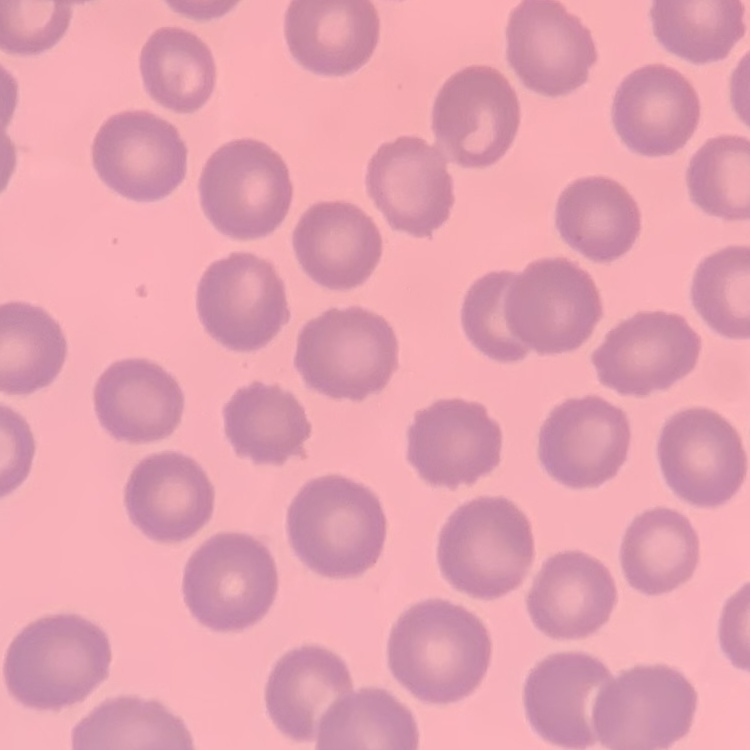

Summary:
  - Erythrocyte morphology: no rouleaux formation
  - Image type: one tile cut from a larger photomicrograph
  - Stain: Field's or Giemsa
  - Preparation: thin blood film